Report the malaria status of this cell.
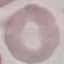
It is uninfected.

Summary:
  - Stain: Giemsa
  - Capture: smartphone camera at the microscope eyepiece
  - Preparation: thin blood smear
  - Image type: cell patch, automatically extracted from a larger field of view and resized to 64 × 64 pixels